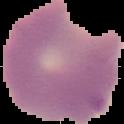

Malaria status: parasitized. The area outside the segmented cell region is set to black. From a thin blood film. Image is 124×124 pixels.